Classify this cell by malaria status.
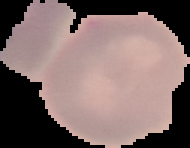
It is uninfected.

Summary:
  - Preparation: thin blood film
  - Image size: 190×148 pixels
  - Image type: segmented cell region with the area outside set to black